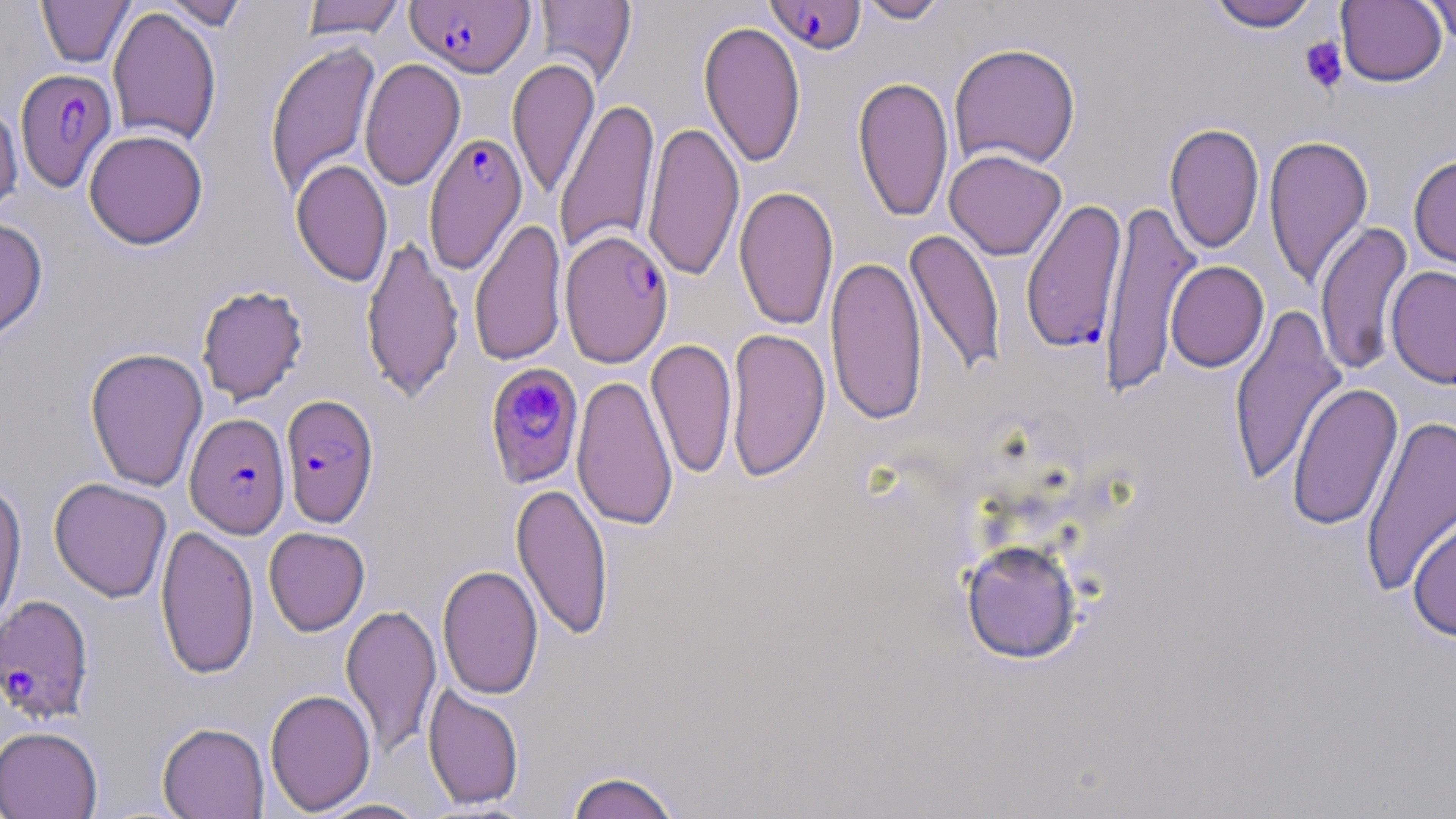
Summary:
  - Coordinate format: approximate bounding boxes as (x1,y1)-(x2,y2) corner pairs in pixels
  - Platelet locations: (1299,36)-(1347,94)
  - Plasmodium falciparum-infected red blood cell locations: (405,0)-(535,77), (764,0)-(868,55), (15,67)-(118,192), (424,131)-(528,273), (1021,198)-(1128,353), (559,228)-(673,367), (485,364)-(585,489), (280,393)-(379,528), (185,412)-(290,538), (0,594)-(94,724)
  - Uninfected red blood cell locations: (36,0)-(134,67), (160,0)-(251,30), (300,0)-(405,40), (856,0)-(950,24), (1206,0)-(1321,32), (1336,0)-(1447,87), (534,1)-(636,88), (1420,1)-(1455,47), (107,6)-(222,147), (698,20)-(806,169), (264,41)-(381,199), (949,42)-(1082,170), (359,57)-(465,191), (507,57)-(599,201), (852,75)-(954,223), (554,97)-(659,257), (0,99)-(23,217), (642,120)-(744,282), (1164,122)-(1264,255), (84,129)-(208,250), (1263,133)-(1374,289), (944,149)-(1067,260), (1408,154)-(1456,272), (291,158)-(392,287), (733,185)-(839,332), (1099,199)-(1201,396), (469,217)-(566,368), (0,218)-(48,343), (1315,220)-(1413,377), (905,228)-(1006,378), (360,233)-(464,404), (825,254)-(927,426), (1165,260)-(1269,372), (1386,265)-(1456,389), (195,283)-(309,406), (1228,304)-(1346,487), (725,327)-(830,483), (646,337)-(737,481), (84,347)-(208,492), (572,374)-(678,531), (1286,382)-(1403,532), (1360,412)-(1455,600), (49,477)-(172,603), (0,479)-(27,631), (511,481)-(614,642), (1407,512)-(1456,642), (155,523)-(259,680), (263,527)-(370,636), (961,539)-(1083,664), (437,564)-(544,700), (341,602)-(441,759), (423,684)-(524,810), (264,688)-(376,816), (157,721)-(269,818), (0,726)-(102,819), (565,769)-(684,818), (313,798)-(430,818)
  - Slide-level diagnosis: Plasmodium falciparum
  - Image size: 1456×819 pixels
  - Stain: May-Grünwald-Giemsa
  - Field of view: one of a larger specimen
  - Preparation: thin blood film
  - Magnification: 1000x
  - Modality: light microscopy